Identify the parasite.
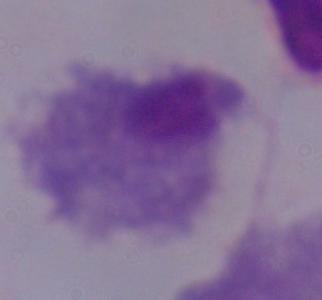

A trichomonad.

{
  "magnification": "1000x",
  "modality": "micrograph"
}